Name the parasite shown.
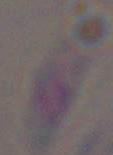
This is Toxoplasma gondii.

magnification: 1000x
modality: micrograph